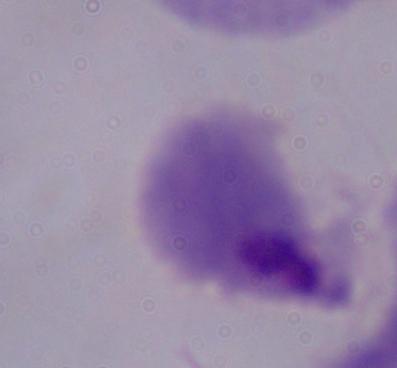
1000x magnification. A trichomonad is seen. Micrograph.